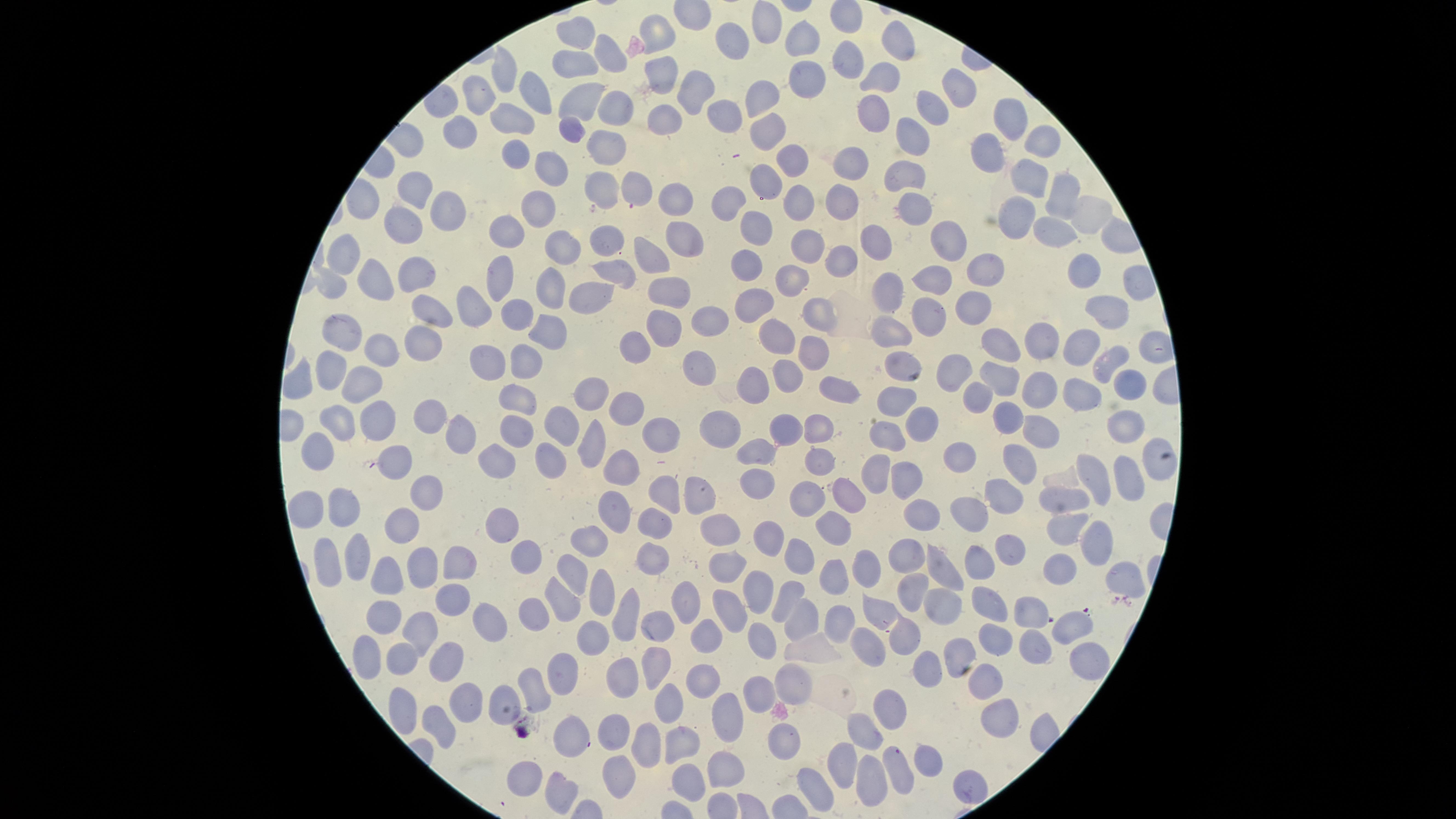

Approximate marker points as (x, y) in pixels.
Summary:
  - Uninfected RBCs: (763, 19), (577, 31), (657, 36), (805, 40), (903, 40), (728, 45), (606, 56), (843, 60), (576, 66), (504, 72), (661, 73), (804, 78), (887, 80), (531, 89), (953, 89), (693, 92), (478, 93), (763, 97), (582, 100), (935, 105), (615, 108), (877, 112), (721, 115), (516, 120), (667, 123), (1011, 123), (573, 128), (769, 128), (460, 134), (919, 134), (1047, 136), (607, 143), (988, 149), (510, 151), (790, 156), (857, 162), (547, 172), (906, 174), (1030, 179), (607, 189), (635, 189), (1063, 192), (410, 194), (674, 199), (844, 200), (726, 202), (918, 203), (799, 208), (542, 210), (445, 211), (1087, 214), (1020, 216), (406, 223), (503, 229), (1057, 232), (753, 234), (683, 238), (876, 239), (604, 243), (955, 243), (807, 246), (561, 249), (335, 250), (645, 255), (838, 257), (748, 261), (413, 267), (1091, 268), (987, 271), (501, 273), (618, 273), (793, 279), (368, 281), (546, 283), (938, 283), (329, 284), (596, 288), (669, 292), (888, 294), (757, 303), (1112, 306), (472, 307), (965, 308), (820, 310), (428, 314), (515, 316), (932, 319), (714, 321), (547, 328), (664, 328), (891, 332), (344, 333), (417, 338), (775, 339), (1045, 344), (634, 348), (378, 349), (993, 349), (815, 351), (1079, 351), (1107, 360), (897, 363), (525, 365), (486, 366), (700, 366), (323, 368), (954, 370), (783, 375), (996, 376), (364, 382), (830, 382), (293, 385), (750, 386), (1079, 389), (1126, 389), (1037, 390), (594, 397), (976, 397), (517, 399), (897, 401), (623, 405), (429, 415), (369, 416), (558, 416), (999, 420), (334, 421), (1128, 422), (916, 424), (721, 426), (514, 427), (815, 427), (1037, 428), (786, 430), (456, 432), (660, 434), (888, 436), (590, 446), (761, 446), (316, 456), (398, 456), (817, 458), (961, 458), (547, 461), (1019, 461), (498, 463), (1156, 464), (623, 465), (873, 475), (1129, 475), (1096, 477), (900, 483), (756, 486), (662, 491), (695, 493), (850, 493), (999, 496), (422, 497), (805, 498), (1063, 498), (609, 506), (304, 507), (337, 508), (923, 512), (968, 514), (655, 521), (405, 524), (1062, 524), (501, 525), (832, 526), (717, 536), (591, 539), (768, 539), (1096, 541), (1004, 550), (353, 552), (526, 553), (901, 554), (653, 557), (795, 557), (327, 561), (976, 562), (942, 565), (420, 567), (455, 567), (867, 567), (383, 569), (728, 569), (1057, 571), (571, 572), (1118, 575), (827, 577), (913, 590), (784, 595), (601, 596), (686, 596), (755, 596), (453, 597), (942, 601), (985, 601), (562, 602), (726, 602), (1030, 608), (625, 611), (878, 612), (382, 616), (533, 616), (801, 618), (836, 620), (1073, 623), (660, 624), (486, 626), (413, 630), (709, 632), (903, 633), (591, 636), (992, 636), (763, 638), (874, 645), (1030, 651), (957, 654), (398, 655), (364, 658), (1083, 660), (443, 663), (921, 666), (649, 670), (618, 674), (559, 675), (791, 676), (532, 681), (700, 683), (981, 687), (504, 693), (755, 694), (667, 700), (458, 701), (886, 706), (403, 719), (723, 721), (996, 721), (436, 728), (866, 732), (609, 733), (577, 736), (678, 739), (780, 739), (640, 745), (839, 762), (924, 763), (723, 771), (520, 772), (869, 772), (612, 774), (686, 777), (965, 781), (563, 788), (815, 790)
  - Parasitized RBCs: (894, 757)
  - Field of view: single
  - Visible region: circular
  - Presence: malaria parasites seen
  - Stain: Giemsa
  - Capture: smartphone photograph through the microscope eyepiece
  - Image size: 1456×819 pixels
  - Species: Plasmodium falciparum
  - Preparation: thin smear of blood